Assess for Plasmodium parasites.
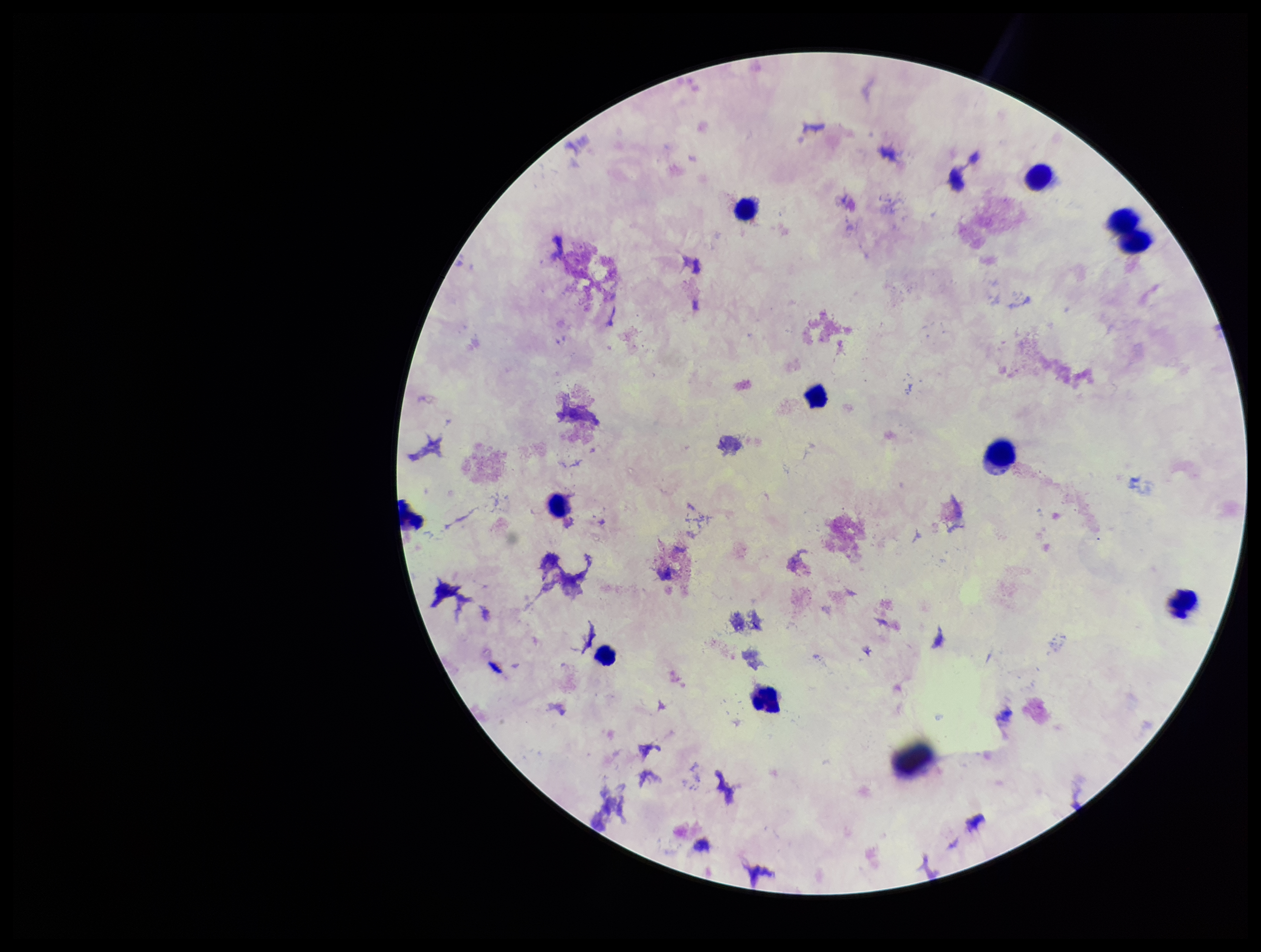
None identified.

Summary:
  - Preparation: thick blood smear
  - Image size: 1261×952 pixels
  - Capture: smartphone photograph through the microscope eyepiece
  - Field of view: single
  - Parasite count: 0
  - Leukocyte count: 10
  - Stain: Giemsa
  - Patient malaria status: negative